Locate every Plasmodium ovale-infected red blood cell.
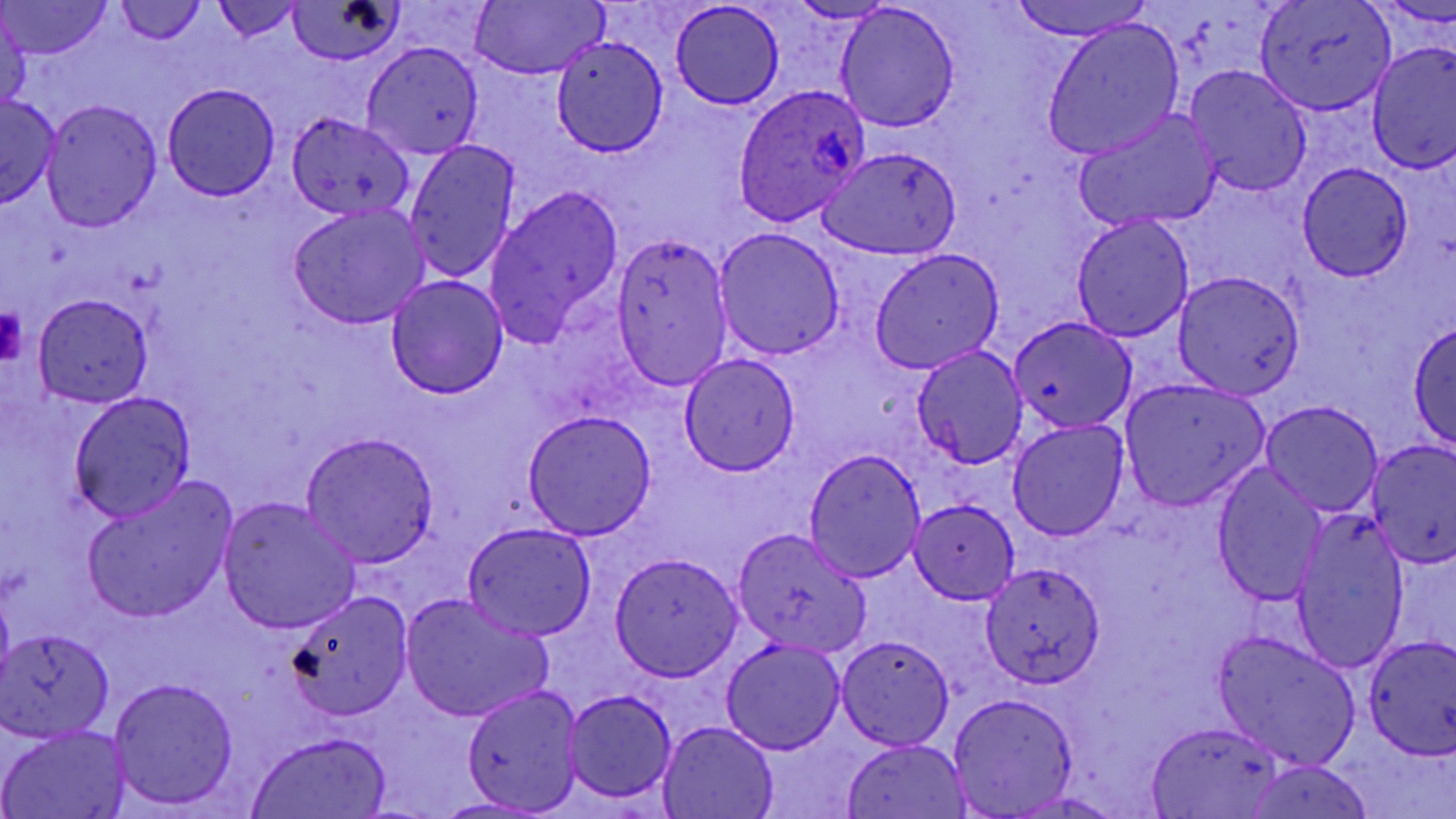

Approximate bounding boxes as (x1, y1, x2, y2) in pixels.
Plasmodium ovale-infected red blood cells: (734, 84, 872, 226).

{
  "slide_level_diagnosis": "Plasmodium ovale",
  "modality": "light microscopy",
  "uninfected_red_blood_cell_locations": "approximate bounding boxes as (x1, y1, x2, y2) in pixels: (3, 0, 111, 59), (289, 0, 403, 65), (1010, 0, 1149, 41), (1255, 0, 1393, 115), (212, 1, 304, 42), (470, 1, 606, 79), (788, 1, 900, 24), (113, 2, 208, 46), (671, 2, 785, 109), (834, 3, 961, 131), (0, 10, 31, 114), (1043, 17, 1186, 159), (551, 36, 669, 156), (362, 42, 483, 160), (1367, 42, 1456, 174), (1184, 65, 1313, 197), (163, 84, 279, 199), (0, 96, 60, 206), (40, 99, 163, 231), (1073, 109, 1221, 232), (287, 111, 415, 225), (404, 137, 521, 285), (818, 144, 963, 260), (1297, 163, 1413, 282), (483, 184, 624, 351), (288, 205, 429, 328), (1071, 214, 1195, 342), (715, 228, 846, 361), (610, 231, 735, 393), (869, 250, 1005, 373), (1172, 271, 1306, 397), (386, 275, 509, 398), (32, 292, 154, 409), (1009, 316, 1138, 434), (1409, 319, 1456, 453), (911, 344, 1028, 468), (677, 354, 801, 477), (1118, 379, 1270, 512), (67, 390, 198, 523), (1260, 400, 1384, 518), (522, 410, 657, 540), (1007, 419, 1129, 542), (300, 432, 439, 565), (1367, 441, 1455, 568), (803, 447, 927, 581), (1211, 465, 1328, 606), (82, 480, 234, 624), (218, 497, 362, 634), (910, 499, 1021, 603), (1290, 512, 1410, 674), (462, 521, 596, 640), (732, 528, 871, 655), (610, 553, 743, 679), (979, 561, 1106, 687), (285, 590, 415, 720), (402, 592, 555, 723), (1, 630, 114, 742), (1211, 631, 1361, 768), (836, 636, 955, 750), (1362, 636, 1456, 757), (721, 638, 844, 754), (108, 676, 240, 811), (461, 684, 584, 813), (563, 690, 677, 803), (946, 692, 1079, 816), (658, 719, 779, 818), (1145, 722, 1285, 816), (1, 725, 129, 818), (247, 733, 390, 817), (843, 739, 972, 817), (1241, 760, 1374, 818), (1010, 791, 1126, 818), (428, 796, 552, 817)",
  "magnification": "1000x",
  "platelet_locations": "approximate bounding boxes as (x1, y1, x2, y2) in pixels: (0, 309, 25, 362)",
  "image_size": "1456×819 pixels",
  "preparation": "thin blood smear",
  "stain": "May-Grünwald-Giemsa",
  "field_of_view": "single"
}